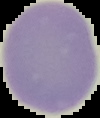
image size = 100×118 pixels
image type = segmented cell region on a black background
result = no Plasmodium parasites detected
preparation = thin blood smear